Assess the morphology of the erythrocytes.
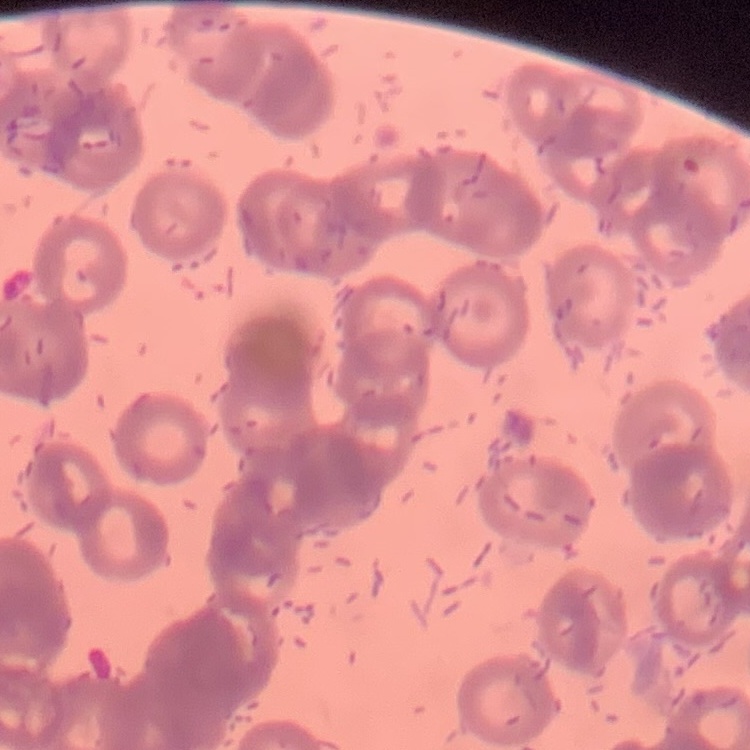

Rouleaux formation.

Thin blood film. One tile cut from a larger photomicrograph. Field's or Giemsa stain.